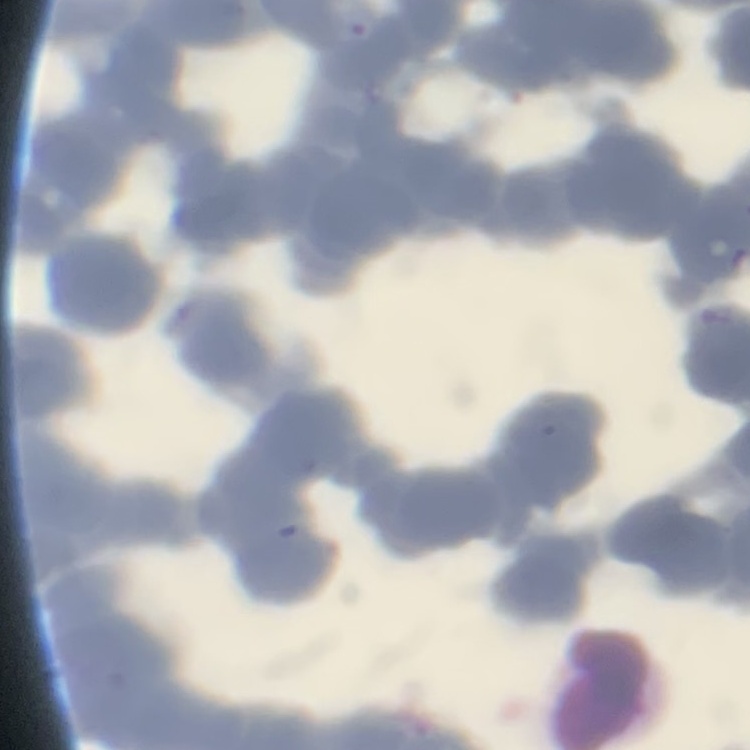
The erythrocytes show rouleaux formation. One tile cut from a larger photomicrograph. Thin blood film. Stained with either Field's or Giemsa.